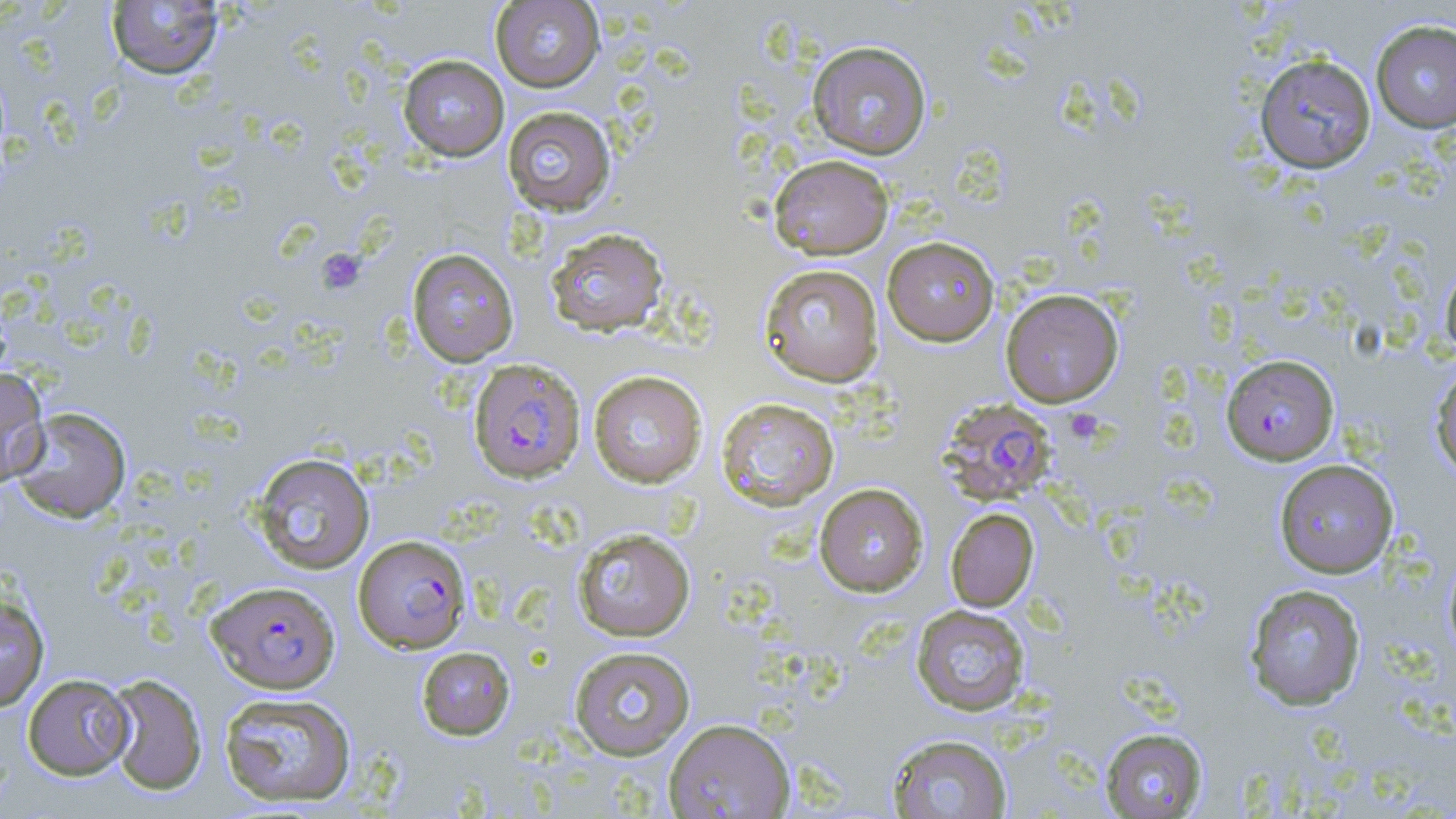
slide-level diagnosis = Plasmodium falciparum
field of view = one of a larger specimen
platelet locations = approximate bounding boxes as named x1/y1/x2/y2 corners in pixels: (x1=317, y1=249, x2=366, y2=295)
magnification = 1000x
modality = optical microscopy
stain = May-Grünwald-Giemsa
uninfected red blood cell locations = approximate bounding boxes as named x1/y1/x2/y2 corners in pixels: (x1=106, y1=1, x2=224, y2=80), (x1=490, y1=1, x2=604, y2=92), (x1=1370, y1=19, x2=1456, y2=133), (x1=807, y1=40, x2=932, y2=159), (x1=1254, y1=53, x2=1376, y2=173), (x1=398, y1=55, x2=509, y2=161), (x1=502, y1=106, x2=617, y2=216), (x1=768, y1=153, x2=895, y2=259), (x1=545, y1=227, x2=670, y2=337), (x1=882, y1=236, x2=1000, y2=346), (x1=406, y1=247, x2=519, y2=366), (x1=1440, y1=260, x2=1456, y2=363), (x1=758, y1=263, x2=884, y2=387), (x1=1000, y1=288, x2=1124, y2=408), (x1=1429, y1=361, x2=1456, y2=482), (x1=0, y1=366, x2=50, y2=487), (x1=588, y1=370, x2=708, y2=488), (x1=715, y1=396, x2=840, y2=512), (x1=9, y1=406, x2=132, y2=523), (x1=250, y1=452, x2=376, y2=574), (x1=1273, y1=459, x2=1400, y2=578), (x1=813, y1=482, x2=928, y2=597), (x1=945, y1=508, x2=1039, y2=612), (x1=571, y1=527, x2=696, y2=642), (x1=1443, y1=549, x2=1456, y2=667), (x1=1244, y1=583, x2=1367, y2=710), (x1=0, y1=594, x2=50, y2=712), (x1=911, y1=604, x2=1031, y2=716), (x1=416, y1=645, x2=515, y2=740), (x1=568, y1=645, x2=696, y2=760), (x1=22, y1=673, x2=134, y2=780), (x1=105, y1=673, x2=207, y2=796), (x1=218, y1=691, x2=357, y2=807), (x1=663, y1=717, x2=795, y2=818), (x1=1100, y1=727, x2=1208, y2=818), (x1=886, y1=733, x2=1013, y2=818)
image size = 1456×819 pixels
preparation = thin blood film
Plasmodium falciparum-infected red blood cell locations = approximate bounding boxes as named x1/y1/x2/y2 corners in pixels: (x1=1221, y1=353, x2=1340, y2=465), (x1=468, y1=358, x2=585, y2=483), (x1=937, y1=397, x2=1058, y2=505), (x1=353, y1=535, x2=472, y2=653), (x1=201, y1=578, x2=335, y2=692)